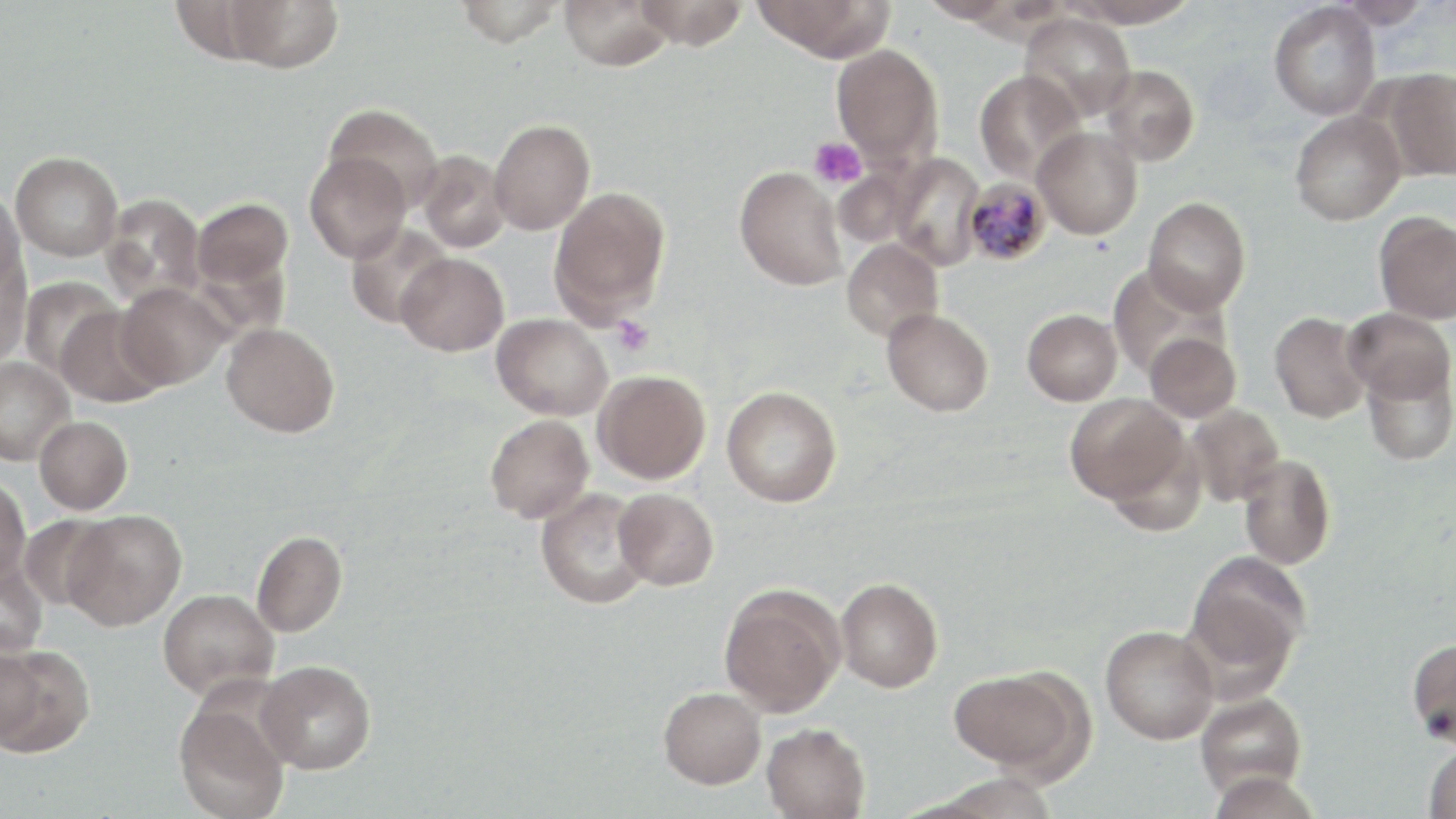

slide_level_diagnosis: Plasmodium malariae
uninfected_red_blood_cell_locations: 'approximate bounding boxes as (x1,y1)-(x2,y2) corner pairs in pixels: (224,0)-(344,72), (454,0)-(564,47), (632,0)-(748,49), (754,0)-(896,60), (919,0)-(1019,24), (1066,0)-(1200,27), (1330,0)-(1433,29), (169,1)-(286,65), (558,1)-(676,70), (1269,1)-(1381,120), (1019,12)-(1136,121), (831,43)-(944,166), (1099,64)-(1199,166), (1379,67)-(1456,182), (974,69)-(1086,183), (323,104)-(444,211), (1289,109)-(1406,225), (489,119)-(595,235), (1033,126)-(1143,239), (416,150)-(511,253), (10,151)-(122,261), (304,151)-(412,263), (888,153)-(985,270), (834,165)-(919,248), (735,166)-(847,291), (549,186)-(671,323), (0,187)-(25,293), (101,194)-(205,306), (192,197)-(293,291), (1143,197)-(1251,314), (1373,210)-(1456,325), (345,222)-(452,328), (841,239)-(943,341), (0,251)-(32,368), (396,253)-(509,356), (1108,263)-(1228,379), (19,276)-(122,378), (117,282)-(231,390), (55,305)-(169,408), (1344,307)-(1456,405), (882,308)-(994,416), (1022,308)-(1123,406), (1269,311)-(1371,423), (492,313)-(612,420), (221,322)-(340,437), (1144,332)-(1242,423), (0,356)-(76,465), (1362,359)-(1456,465), (592,369)-(711,484), (722,386)-(842,507), (1065,393)-(1187,504), (1185,403)-(1284,506), (485,413)-(594,523), (34,415)-(133,514), (1100,429)-(1208,536), (1238,453)-(1336,570), (0,475)-(30,585), (535,488)-(654,609), (613,488)-(718,591), (62,509)-(186,631), (18,515)-(115,610), (251,530)-(348,637), (1186,552)-(1309,676), (0,557)-(48,657), (835,577)-(943,692), (718,583)-(846,717), (157,588)-(279,700), (1100,624)-(1219,744), (1407,637)-(1456,746), (1,643)-(46,749), (0,644)-(94,757), (257,659)-(376,774), (948,667)-(1084,776), (659,687)-(766,789), (1195,691)-(1307,799), (173,701)-(290,819), (762,722)-(870,819), (1423,744)-(1456,819)'
image_size: 1456×819 pixels
stain: May-Grünwald-Giemsa
plasmodium_malariae_infected_red_blood_cell_locations: 'approximate bounding boxes as (x1,y1)-(x2,y2) corner pairs in pixels: (962,177)-(1051,266)'
modality: light microscopy
field_of_view: one of a larger specimen
platelet_locations: 'approximate bounding boxes as (x1,y1)-(x2,y2) corner pairs in pixels: (809,137)-(867,190), (610,315)-(654,356)'
magnification: 1000x
preparation: thin blood smear